Outline each Plasmodium falciparum-infected red blood cell.
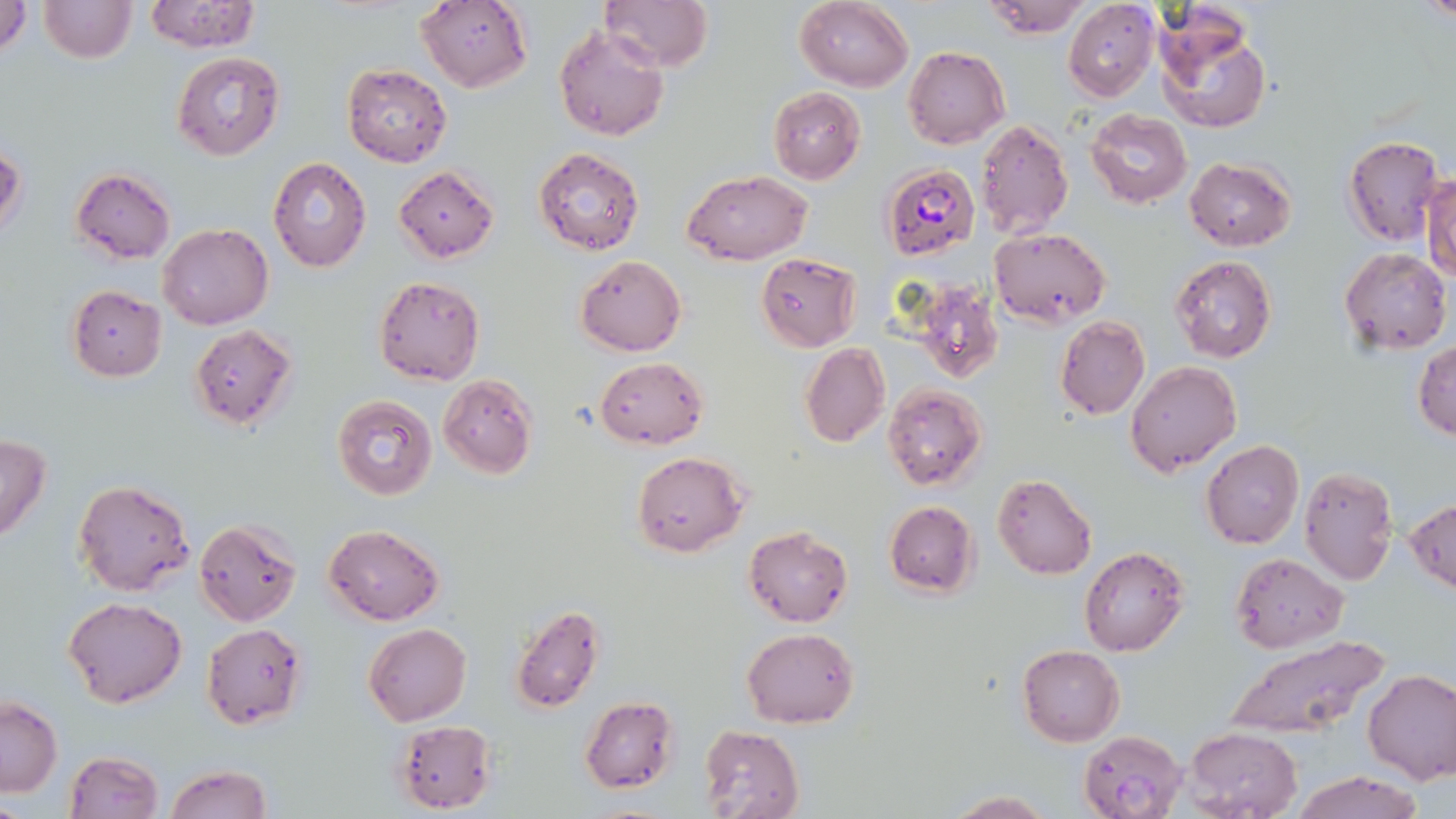
Approximate bounding boxes as (x1, y1, x2, y2) in pixels.
Plasmodium falciparum-infected red blood cells: (881, 163, 979, 260).

Summary:
  - Uninfected red blood cell locations: (37, 0, 136, 64), (141, 0, 261, 53), (414, 0, 533, 92), (599, 0, 713, 72), (793, 0, 914, 90), (980, 0, 1093, 39), (1062, 0, 1162, 102), (1, 1, 32, 59), (1153, 9, 1272, 134), (554, 25, 670, 143), (901, 46, 1009, 149), (172, 52, 285, 160), (341, 63, 452, 167), (767, 87, 867, 183), (1084, 109, 1193, 209), (975, 120, 1073, 238), (1342, 135, 1447, 246), (0, 145, 27, 243), (534, 146, 645, 257), (1185, 156, 1298, 252), (268, 158, 372, 272), (393, 166, 500, 262), (70, 168, 176, 264), (1424, 169, 1456, 283), (685, 172, 811, 266), (157, 224, 273, 330), (989, 226, 1112, 326), (1339, 247, 1451, 355), (756, 252, 864, 351), (575, 254, 686, 356), (1169, 257, 1278, 364), (373, 276, 485, 386), (66, 286, 167, 381), (913, 286, 1004, 384), (1056, 315, 1151, 419), (189, 324, 298, 431), (1413, 340, 1456, 440), (801, 342, 890, 449), (595, 357, 707, 448), (1125, 360, 1242, 477), (438, 374, 538, 478), (882, 383, 987, 491), (331, 395, 438, 500), (0, 434, 53, 544), (1201, 440, 1304, 550), (632, 451, 747, 556), (1299, 464, 1399, 586), (992, 472, 1097, 579), (71, 479, 194, 596), (1406, 498, 1456, 597), (885, 501, 980, 598), (193, 518, 302, 626), (324, 524, 444, 624), (743, 526, 853, 628), (1079, 546, 1189, 657), (1230, 552, 1347, 655), (64, 596, 185, 708), (507, 603, 606, 713), (201, 622, 308, 730), (363, 623, 472, 726), (742, 628, 859, 728), (1219, 632, 1395, 745), (1016, 645, 1125, 747), (1362, 668, 1456, 784), (580, 695, 679, 792), (0, 696, 61, 799), (391, 719, 497, 814), (698, 726, 804, 819), (1182, 726, 1302, 818), (1079, 729, 1189, 819), (64, 751, 163, 819), (165, 764, 272, 819), (1291, 772, 1425, 819), (945, 791, 1056, 819)
  - Slide-level diagnosis: Plasmodium falciparum
  - Magnification: 1000x
  - Field of view: one of a larger specimen
  - Image size: 1456×819 pixels
  - Stain: May-Grünwald-Giemsa
  - Modality: optical microscopy
  - Preparation: thin blood smear